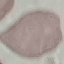
Summary:
  - Malaria status: uninfected
  - Image type: cell patch, automatically extracted from a larger field of view and resized to 64 × 64 pixels
  - Stain: Giemsa
  - Capture: smartphone camera at the microscope eyepiece
  - Preparation: thin blood smear